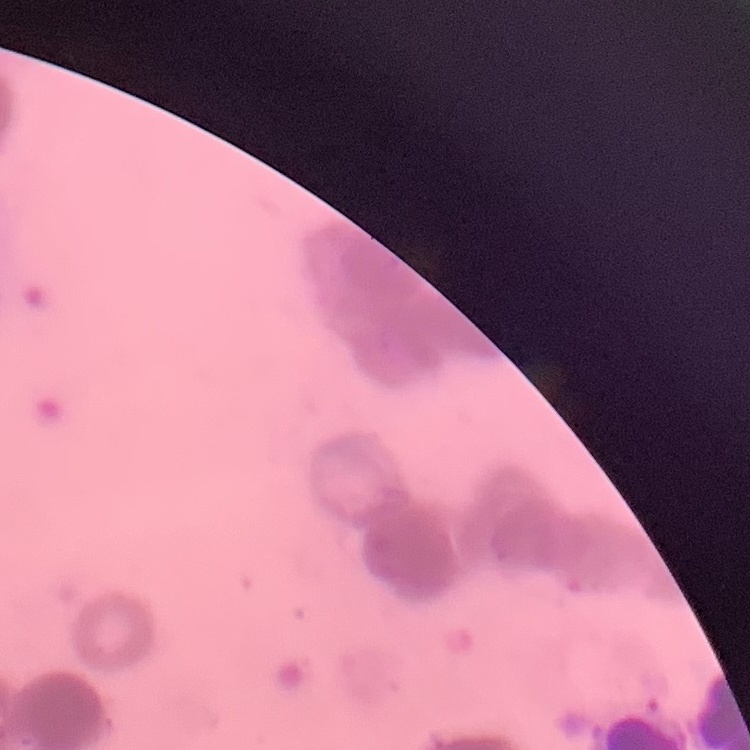

{
  "red_blood_cell_morphology": "rouleaux formation",
  "preparation": "thin peripheral smear",
  "stain": "Field's or Giemsa",
  "image_type": "one tile cut from a larger photomicrograph"
}